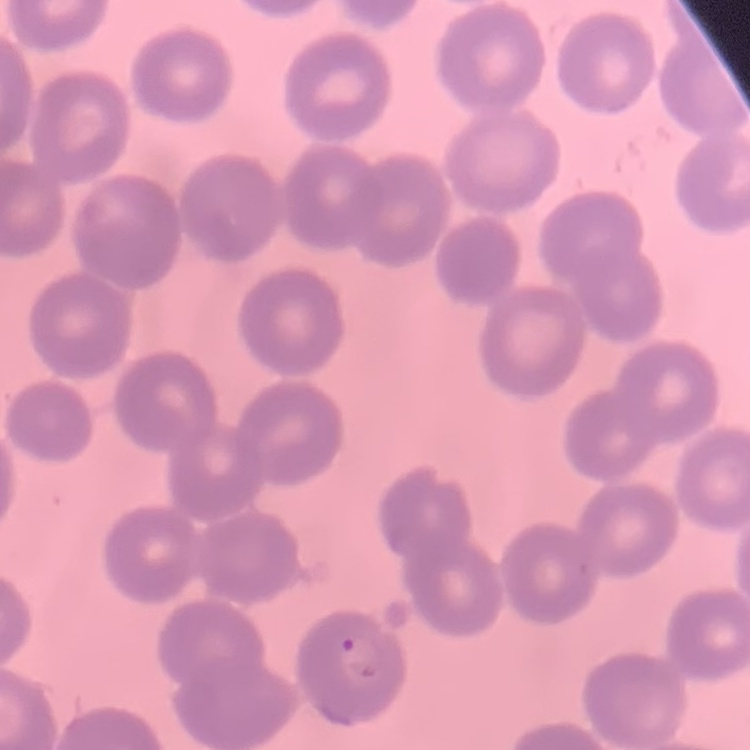

Summary:
  - Erythrocyte morphology: no rouleaux formation
  - Image type: square crop of a larger photomicrograph
  - Preparation: thin blood film
  - Stain: Field's or Giemsa